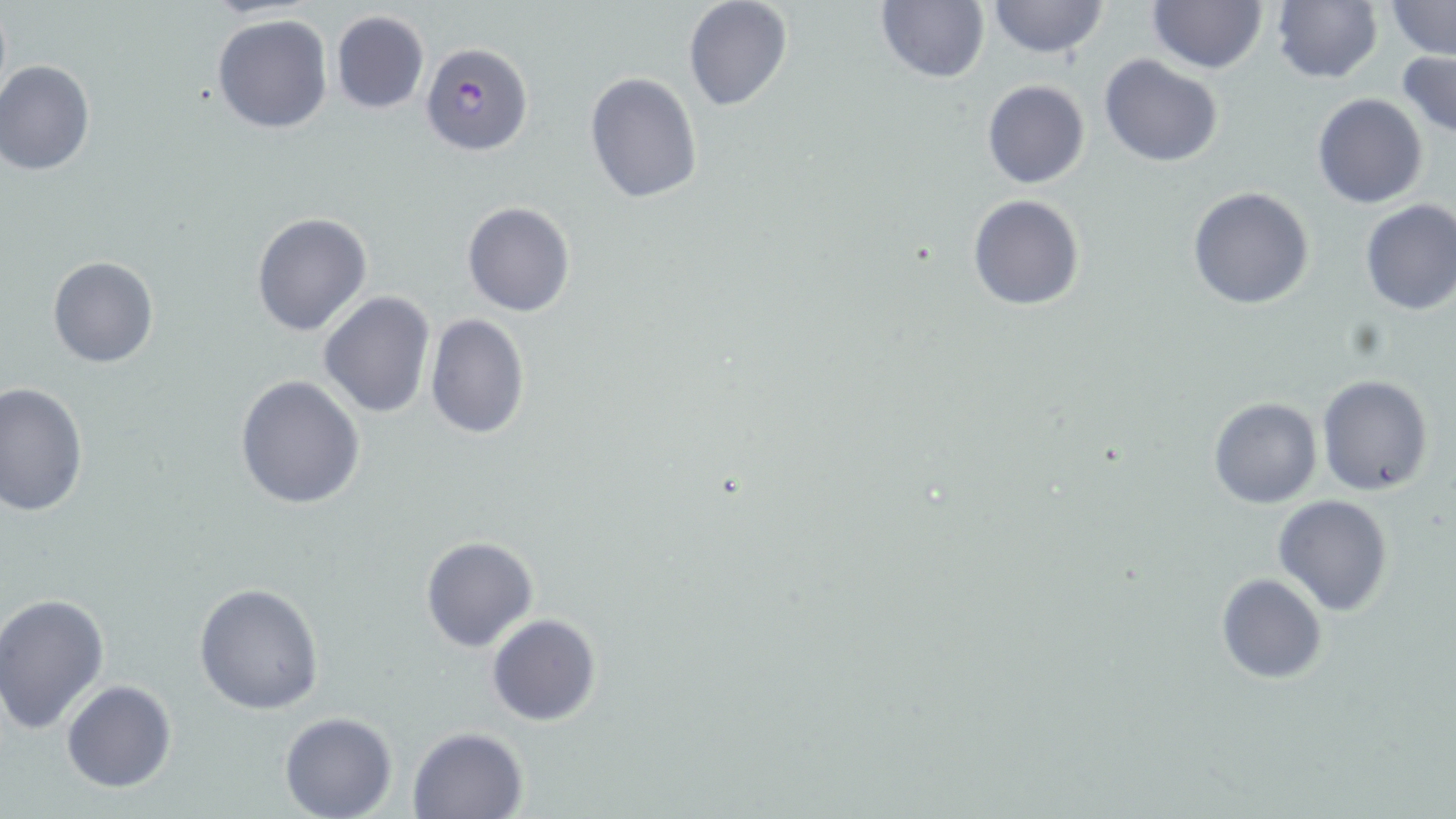

Approximate bounding boxes as (x1, y1, x2, y2) in pixels. Plasmodium falciparum-infected red blood cell locations: (420, 42, 535, 157). Uninfected red blood cell locations: (681, 0, 794, 113), (876, 0, 990, 84), (986, 0, 1110, 60), (1147, 0, 1269, 75), (872, 2, 1112, 74), (1269, 2, 1384, 84), (1387, 2, 1453, 59), (329, 10, 431, 115), (211, 12, 335, 134), (1399, 48, 1456, 141), (1098, 54, 1223, 168), (0, 60, 96, 175), (584, 72, 704, 206), (982, 79, 1090, 189), (1312, 93, 1428, 208), (1187, 186, 1315, 310), (968, 194, 1085, 311), (1357, 198, 1456, 315), (462, 202, 576, 317), (252, 211, 374, 336), (47, 255, 158, 368), (318, 292, 434, 418), (425, 313, 529, 441), (234, 374, 367, 509), (1316, 374, 1434, 497), (0, 383, 88, 519), (1208, 396, 1323, 509), (1272, 494, 1394, 615), (421, 537, 539, 653), (1216, 573, 1327, 683), (192, 582, 324, 716), (0, 594, 110, 734), (487, 613, 602, 727), (61, 680, 178, 793), (280, 710, 397, 818), (408, 725, 529, 817). Slide-level diagnosis: Plasmodium falciparum. Light microscopy. Single field of view. Captured at 1000x magnification. Image is 1456×819 pixels. Thin blood smear. May-Grünwald-Giemsa stain.